Identify the parasite.
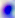
Toxoplasma gondii.

400x magnification. Micrograph.